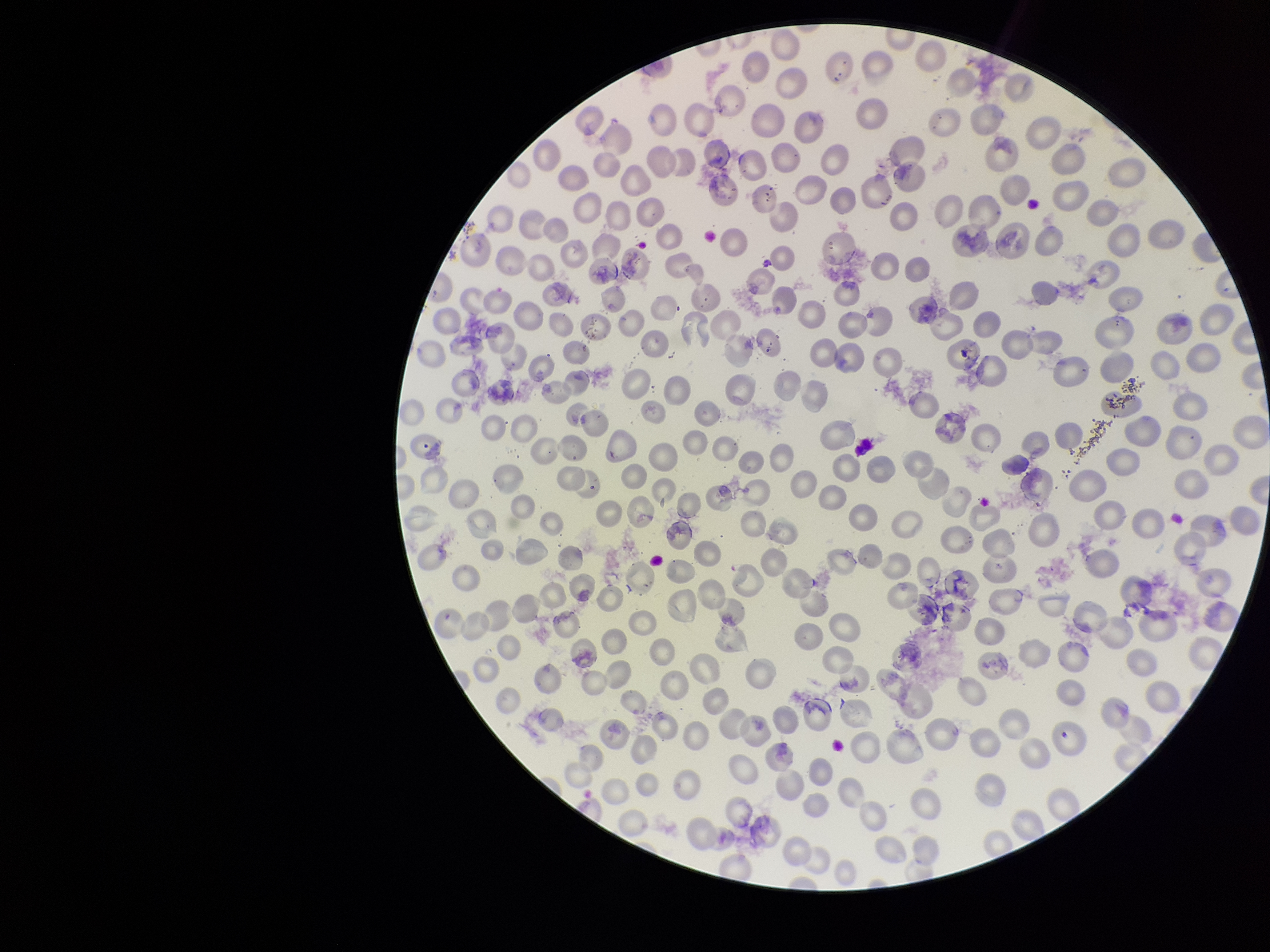
Summary:
  - Preparation: thin smear
  - Field of view: one from this slide
  - Stain: Giemsa
  - Parasitized red blood cell count: 0
  - Capture: smartphone photograph through the microscope eyepiece
  - Patient malaria status: infected
  - Parasitized red blood cells: none seen
  - Image size: 1270×952 pixels
  - Species reported for this patient: Plasmodium vivax
  - Red blood cell count: 259